Classify this cell by malaria status.
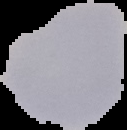
It is uninfected.

preparation = thin blood film
image type = cell region segmented out of the field of view; surrounding area masked to black
image size = 127×130 pixels